Give the preparation type.
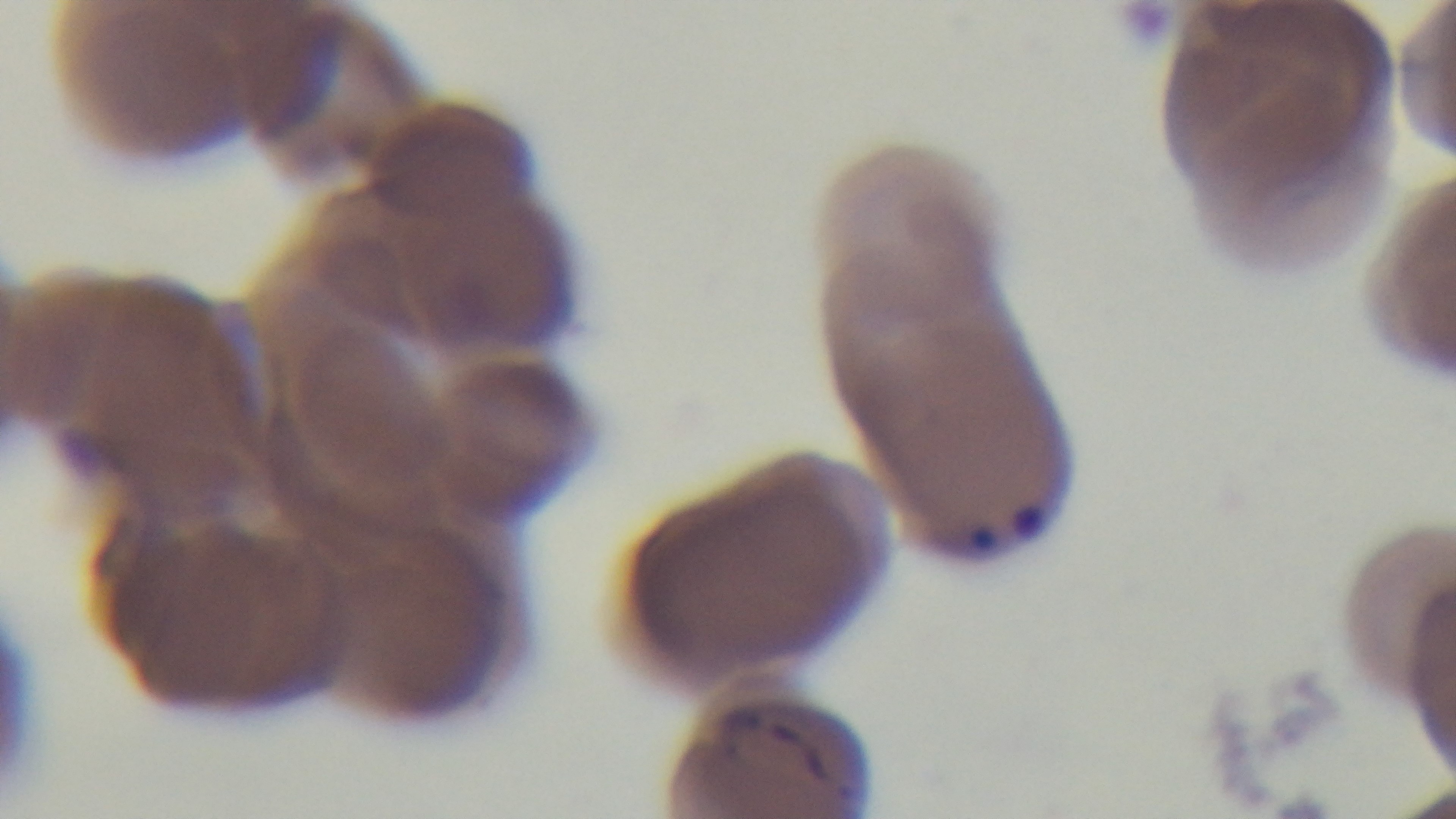

A thin smear.

field of view = single
objective = 100x oil immersion
stain = Giemsa
modality = light microscopy
malaria status = infected
capture = mounted 4K digital camera